Assess this cell for malaria.
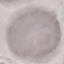

Uninfected.

Summary:
  - Image type: cell patch, automatically extracted from a larger field of view and resized to 64 × 64 pixels
  - Preparation: thin blood smear
  - Stain: Giemsa
  - Capture: smartphone camera at the microscope eyepiece